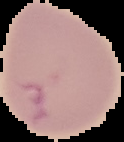

image size = 124×142 pixels
image type = cell region segmented out of the field of view; surrounding area masked to black
preparation = thin blood film
result = malaria parasites detected